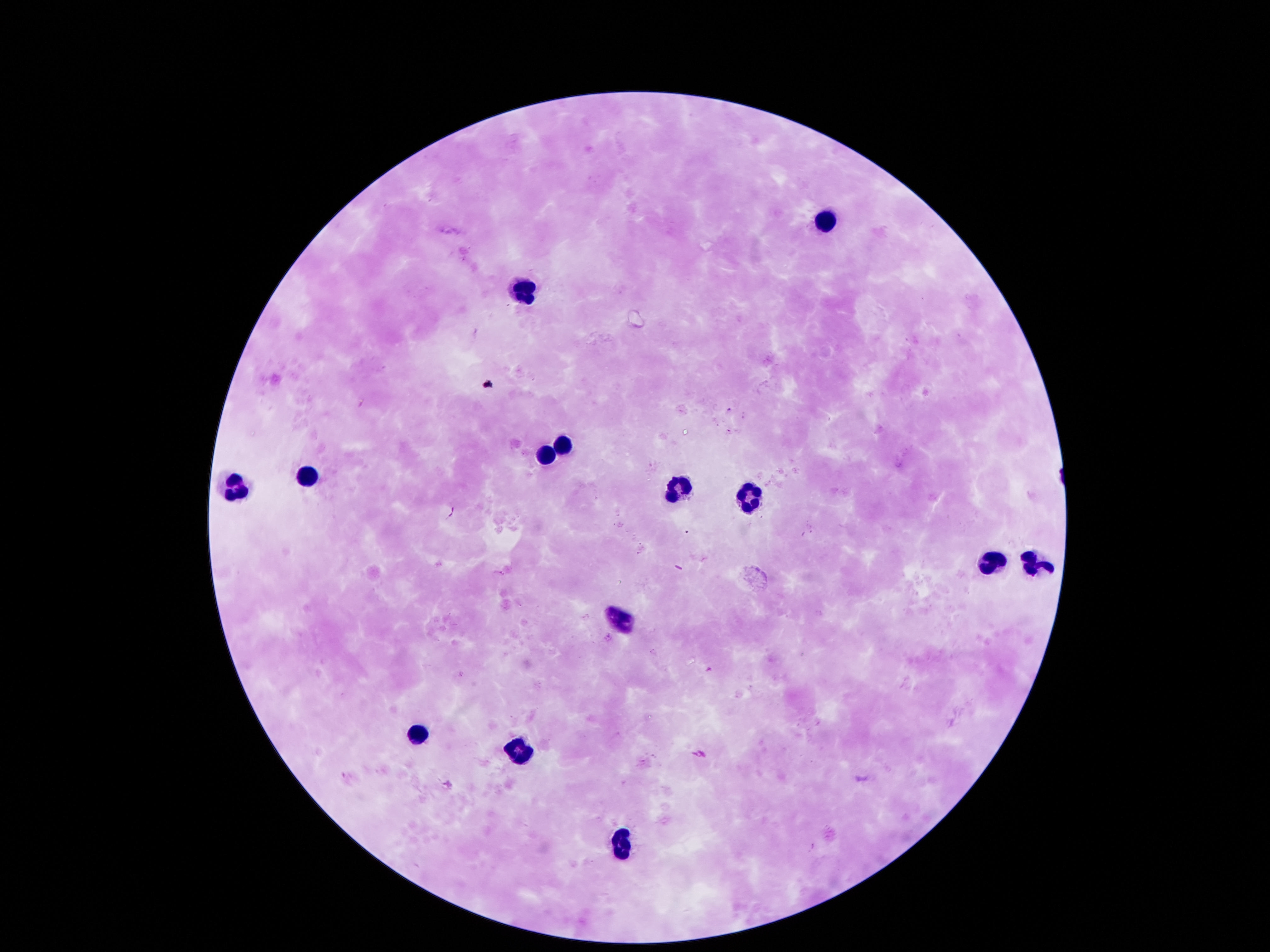
Approximate centers as {x, y} in pixels.
Summary:
  - Leukocyte locations: {820, 219}, {524, 288}, {561, 442}, {545, 455}, {306, 473}, {232, 489}, {746, 492}, {679, 495}, {988, 560}, {1029, 566}, {619, 617}, {417, 735}, {521, 750}, {622, 838}
  - Capture: smartphone camera through the microscope eyepiece
  - Stain: Giemsa
  - Preparation: thick blood film
  - Patient malaria status: uninfected
  - Field of view: one from this slide
  - Magnification: 100x
  - Image size: 1270×952 pixels